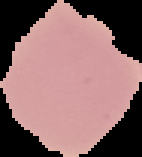

image size = 142×157 pixels
image type = cell region segmented out of the field of view; surrounding area masked to black
result = negative for malaria parasites
preparation = thin blood film